Name the blood parasite species.
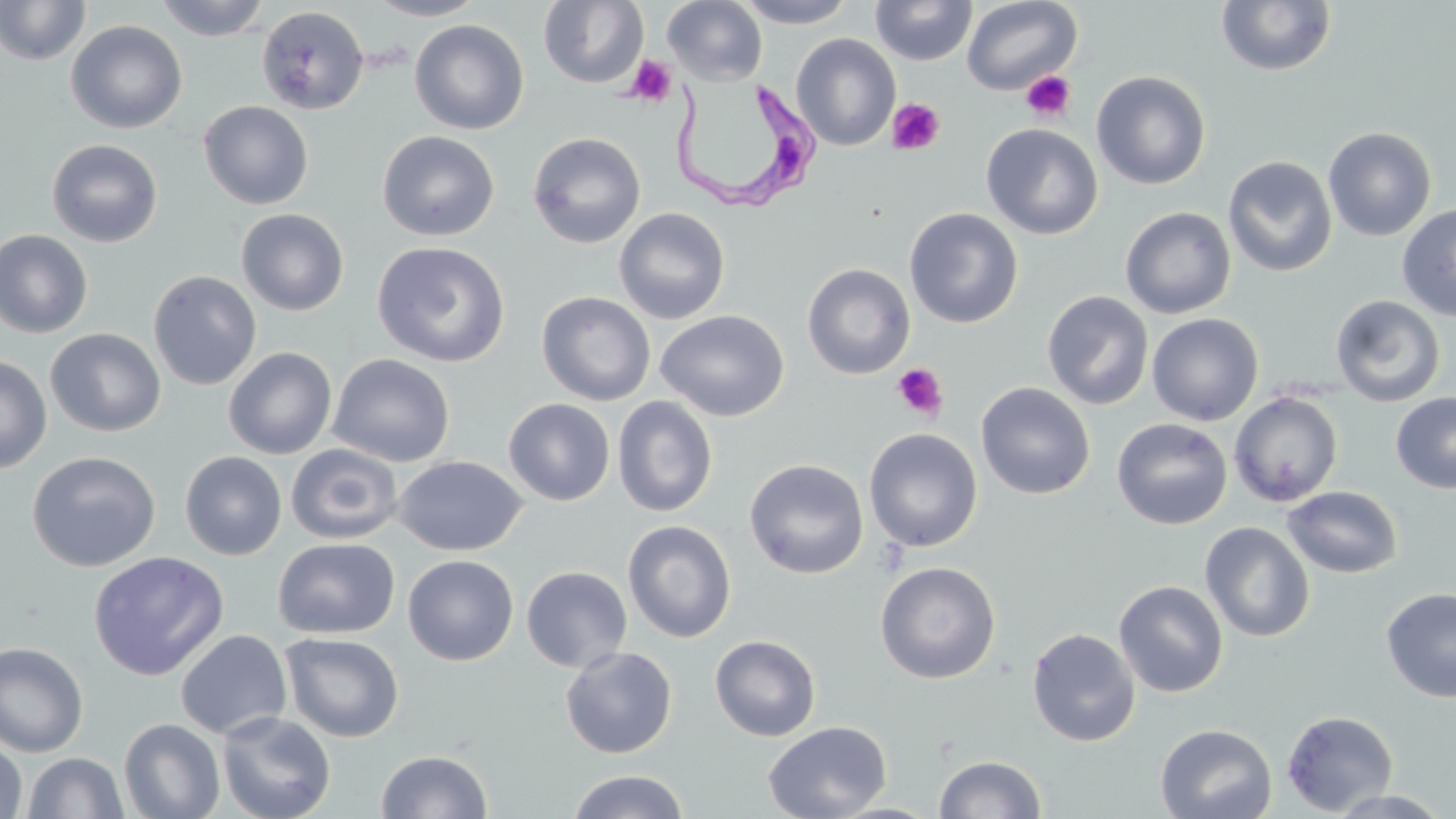
Trypanosoma brucei.

Summary:
  - Coordinate format: approximate bounding boxes as (x1,y1)-(x2,y2) corner pairs in pixels
  - Platelet locations: (625,55)-(677,107), (1020,70)-(1076,123), (886,98)-(945,155), (892,363)-(948,420)
  - Trypanosoma brucei locations: (664,78)-(824,216)
  - Uninfected red blood cell locations: (154,0)-(272,41), (366,0)-(488,21), (538,0)-(648,88), (662,0)-(767,86), (734,0)-(860,28), (870,0)-(977,66), (961,0)-(1083,95), (0,1)-(91,66), (1215,1)-(1338,76), (256,6)-(369,115), (65,19)-(187,134), (409,19)-(529,135), (791,33)-(901,151), (1091,70)-(1211,189), (198,100)-(314,210), (981,123)-(1103,239), (1322,126)-(1436,241), (376,130)-(500,241), (528,131)-(646,249), (46,138)-(163,247), (1222,155)-(1338,277), (1396,205)-(1456,321), (613,206)-(731,324), (1120,206)-(1236,319), (903,207)-(1023,328), (236,208)-(349,316), (1,229)-(93,338), (371,240)-(510,367), (802,262)-(915,379), (148,270)-(262,390), (536,291)-(655,406), (1042,291)-(1154,409), (1329,294)-(1446,408), (654,309)-(790,422), (1146,312)-(1264,426), (45,328)-(166,437), (223,346)-(337,459), (327,353)-(455,467), (0,354)-(52,473), (976,381)-(1095,499), (1228,391)-(1344,507), (1391,392)-(1456,494), (612,396)-(718,518), (503,397)-(615,506), (1111,417)-(1232,530), (864,427)-(983,552), (286,443)-(403,544), (26,451)-(161,572), (180,451)-(287,560), (393,454)-(526,556), (744,458)-(869,579), (1282,485)-(1403,579), (622,519)-(736,642), (1199,521)-(1315,642), (273,537)-(400,639), (88,550)-(230,680), (403,554)-(519,665), (875,561)-(1001,683), (521,565)-(633,673), (1114,580)-(1229,698), (1381,587)-(1456,702), (1026,627)-(1140,747), (175,629)-(293,740), (279,632)-(404,742), (709,634)-(821,741), (0,642)-(88,758), (559,645)-(678,759), (1281,709)-(1399,816), (217,712)-(336,819), (119,718)-(225,819), (763,720)-(892,819), (1154,723)-(1277,819), (0,738)-(28,819), (376,749)-(493,818), (23,751)-(129,818), (933,754)-(1046,818), (568,769)-(690,819), (1327,789)-(1452,818)
  - Field of view: single
  - Magnification: 1000x
  - Modality: optical microscopy
  - Stain: May-Grünwald-Giemsa
  - Preparation: thin blood smear
  - Image size: 1456×819 pixels